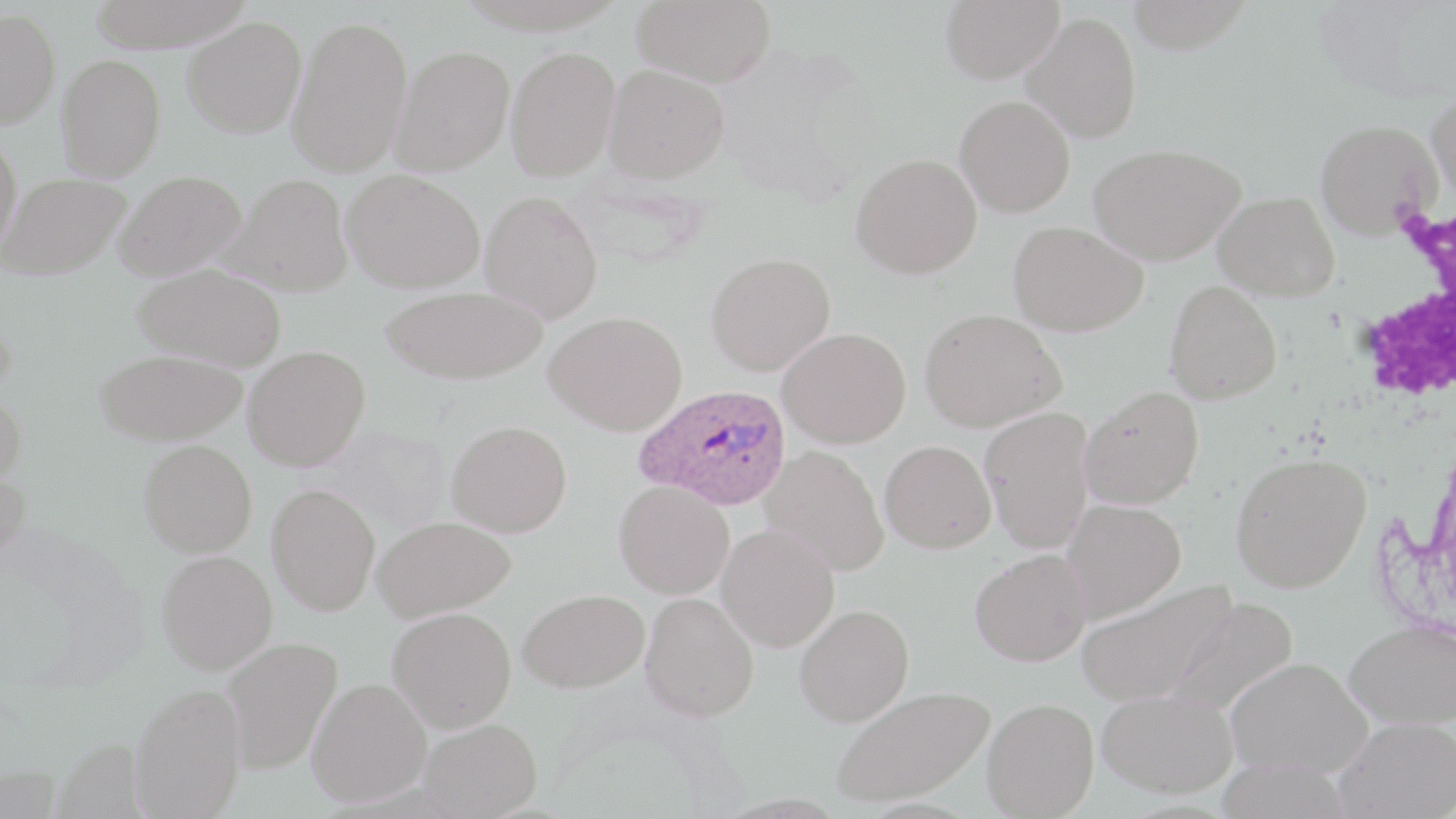
slide_level_diagnosis: Plasmodium ovale
white_blood_cell_locations: 'approximate bounding boxes as (x1,y1)-(x2,y2) corner pairs in pixels: (1345,194)-(1456,423)'
plasmodium_ovale_infected_red_blood_cell_locations: 'approximate bounding boxes as (x1,y1)-(x2,y2) corner pairs in pixels: (635,384)-(792,511)'
image_size: 1456×819 pixels
field_of_view: single
modality: optical microscopy
uninfected_red_blood_cell_locations: 'approximate bounding boxes as (x1,y1)-(x2,y2) corner pairs in pixels: (85,0)-(258,51), (632,0)-(777,87), (940,0)-(1063,83), (1126,0)-(1255,54), (0,8)-(60,129), (1022,11)-(1142,143), (287,14)-(413,177), (182,16)-(307,138), (390,46)-(514,175), (505,46)-(620,181), (56,53)-(166,181), (604,65)-(730,183), (1427,90)-(1456,210), (955,95)-(1075,218), (1315,119)-(1441,239), (0,131)-(23,261), (1089,143)-(1243,265), (850,153)-(982,279), (342,169)-(485,293), (113,170)-(246,281), (1,173)-(131,279), (219,174)-(353,297), (480,190)-(603,322), (1213,191)-(1340,300), (1008,220)-(1148,336), (705,252)-(835,376), (133,262)-(287,371), (1165,280)-(1283,404), (380,286)-(548,384), (920,308)-(1065,432), (544,311)-(687,435), (777,327)-(911,448), (243,345)-(370,471), (94,348)-(246,446), (1078,385)-(1204,509), (0,390)-(27,490), (979,406)-(1095,554), (447,419)-(572,537), (138,439)-(257,557), (879,440)-(996,553), (760,445)-(889,576), (1229,452)-(1371,592), (0,468)-(31,575), (614,481)-(734,599), (266,483)-(380,616), (1061,498)-(1186,621), (371,515)-(515,622), (716,524)-(839,652), (970,548)-(1091,666), (156,550)-(278,675), (1076,577)-(1237,707), (517,588)-(649,693), (640,592)-(760,721), (1159,594)-(1298,717), (794,604)-(914,727), (387,607)-(516,732), (1343,620)-(1456,729), (220,636)-(344,775), (1224,656)-(1372,778), (308,678)-(432,807), (130,682)-(247,818), (830,685)-(994,807), (1097,687)-(1237,797), (982,698)-(1099,818), (1335,717)-(1455,819), (417,718)-(543,818)'
magnification: 1000x
stain: May-Grünwald-Giemsa
preparation: thin blood smear